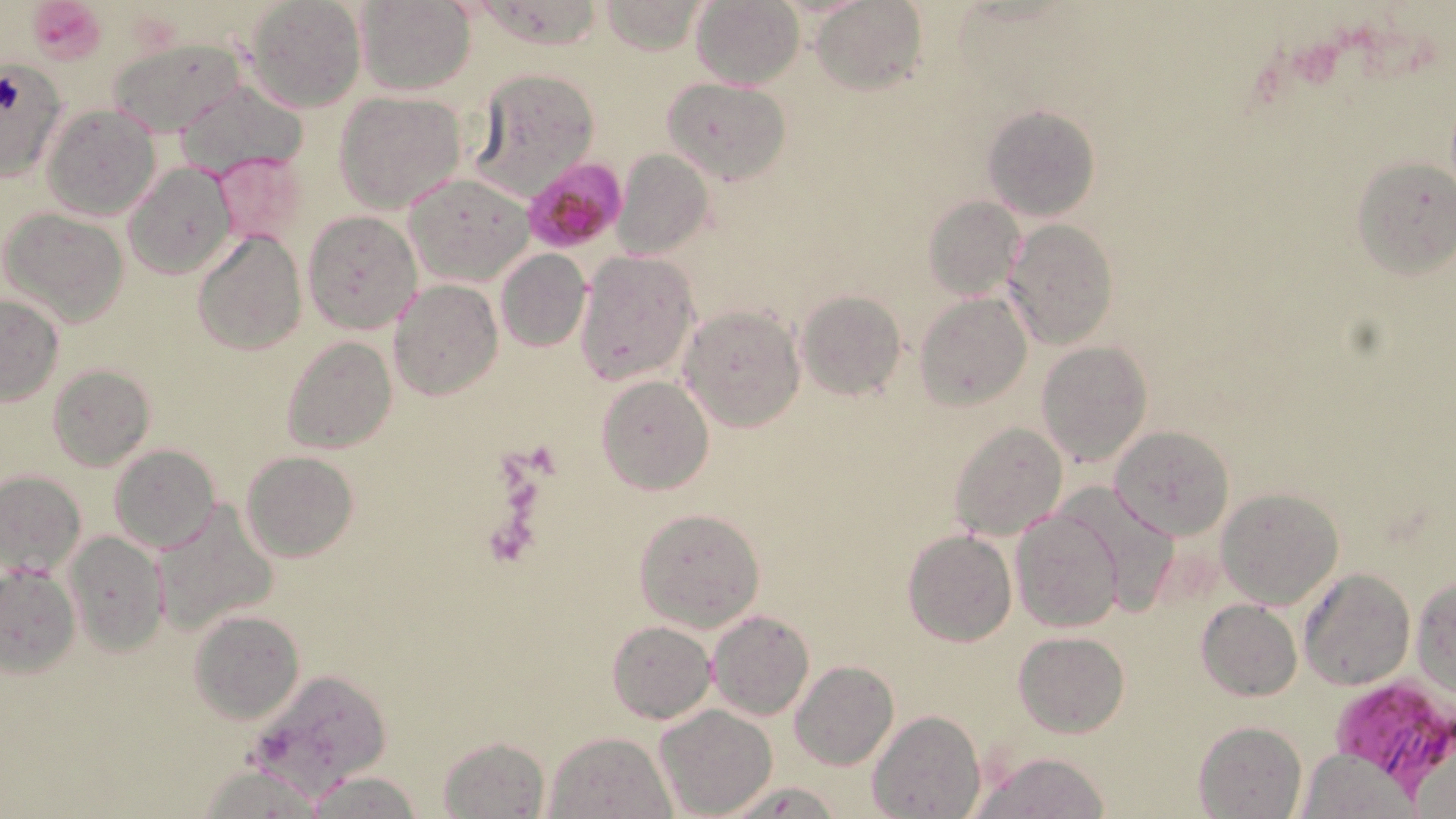

Summary:
  - Coordinate format: approximate bounding boxes as (x1,y1)-(x2,y2) corner pairs in pixels
  - Platelet locations: (27,0)-(108,64), (483,518)-(531,567)
  - Uninfected red blood cell locations: (242,0)-(365,114), (356,0)-(475,96), (691,0)-(803,89), (599,1)-(706,55), (812,1)-(926,96), (106,37)-(250,139), (0,56)-(69,183), (468,66)-(598,199), (661,77)-(790,185), (174,80)-(307,179), (334,90)-(467,213), (42,105)-(159,221), (982,105)-(1102,222), (612,148)-(712,261), (209,149)-(311,251), (1350,157)-(1456,279), (123,162)-(238,281), (404,173)-(533,287), (923,196)-(1027,301), (3,209)-(129,328), (302,211)-(422,334), (1003,219)-(1118,351), (191,229)-(307,357), (495,248)-(591,352), (576,252)-(699,386), (389,280)-(503,403), (796,289)-(906,400), (916,291)-(1031,410), (0,294)-(64,406), (680,305)-(804,431), (282,336)-(397,454), (1036,341)-(1153,468), (47,363)-(155,470), (597,375)-(714,496), (950,420)-(1069,540), (1109,425)-(1235,541), (109,445)-(221,554), (242,451)-(358,561), (0,469)-(87,580), (1058,483)-(1180,608), (1215,487)-(1344,607), (151,500)-(279,637), (634,507)-(766,632), (1011,507)-(1123,632), (901,528)-(1017,646), (66,530)-(167,656), (0,563)-(78,676), (1298,567)-(1415,689), (1412,573)-(1455,697), (1197,600)-(1302,700), (189,610)-(306,724), (706,610)-(816,721), (606,619)-(716,724), (1016,632)-(1129,738), (790,660)-(898,770), (655,704)-(777,817), (867,710)-(984,819), (1193,720)-(1308,818), (542,730)-(676,818), (437,735)-(549,817), (1301,748)-(1419,817), (970,750)-(1112,819), (197,764)-(332,816), (305,772)-(422,819), (722,778)-(842,819)
  - Plasmodium falciparum-infected red blood cell locations: (523,157)-(629,255), (1324,679)-(1456,793)
  - Slide-level diagnosis: Plasmodium falciparum
  - Image size: 1456×819 pixels
  - Preparation: thin blood film
  - Stain: May-Grünwald-Giemsa
  - Modality: light microscopy
  - Magnification: 1000x
  - Field of view: one of a larger specimen